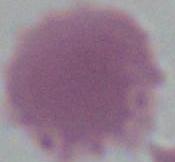

{
  "modality": "photomicrograph",
  "magnification": "1000x",
  "identification": "erythrocyte"
}